State which parasite is depicted.
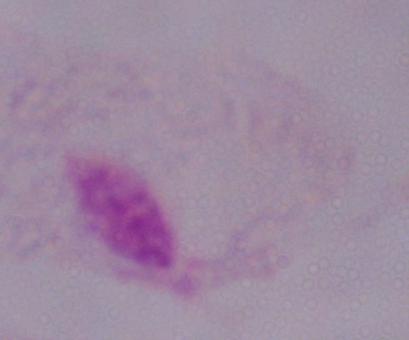
A trichomonad.

Summary:
  - Magnification: 1000x
  - Modality: micrograph